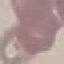
Malaria status: uninfected. Acquired by smartphone through the microscope eyepiece. Giemsa stain. Cell patch, automatically extracted from a larger field of view and resized to 64 × 64 pixels. Thin blood film.